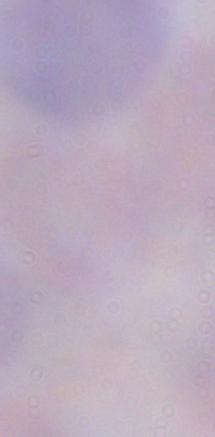 Micrograph. 1000x magnification. A trypanosome is seen.